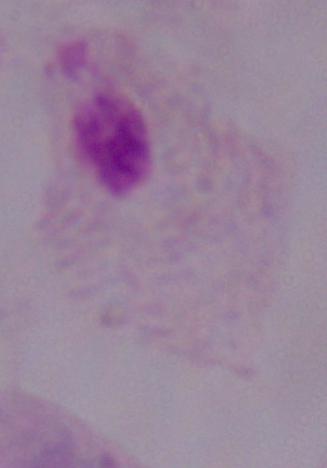

identification: trichomonad
magnification: 1000x
modality: micrograph